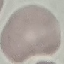
Summary:
  - Result: no malaria parasites seen
  - Image type: automatically extracted cell patch, resized to 64 × 64 pixels
  - Preparation: thin blood film
  - Capture: smartphone camera at the microscope eyepiece
  - Stain: Giemsa